Report the malaria status of this cell.
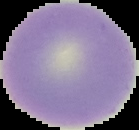
Uninfected.

From a thin blood smear. Image is 139×130 pixels. Cell region segmented out of the field of view; the surrounding area is masked to black.